Locate and identify every blood parasite.
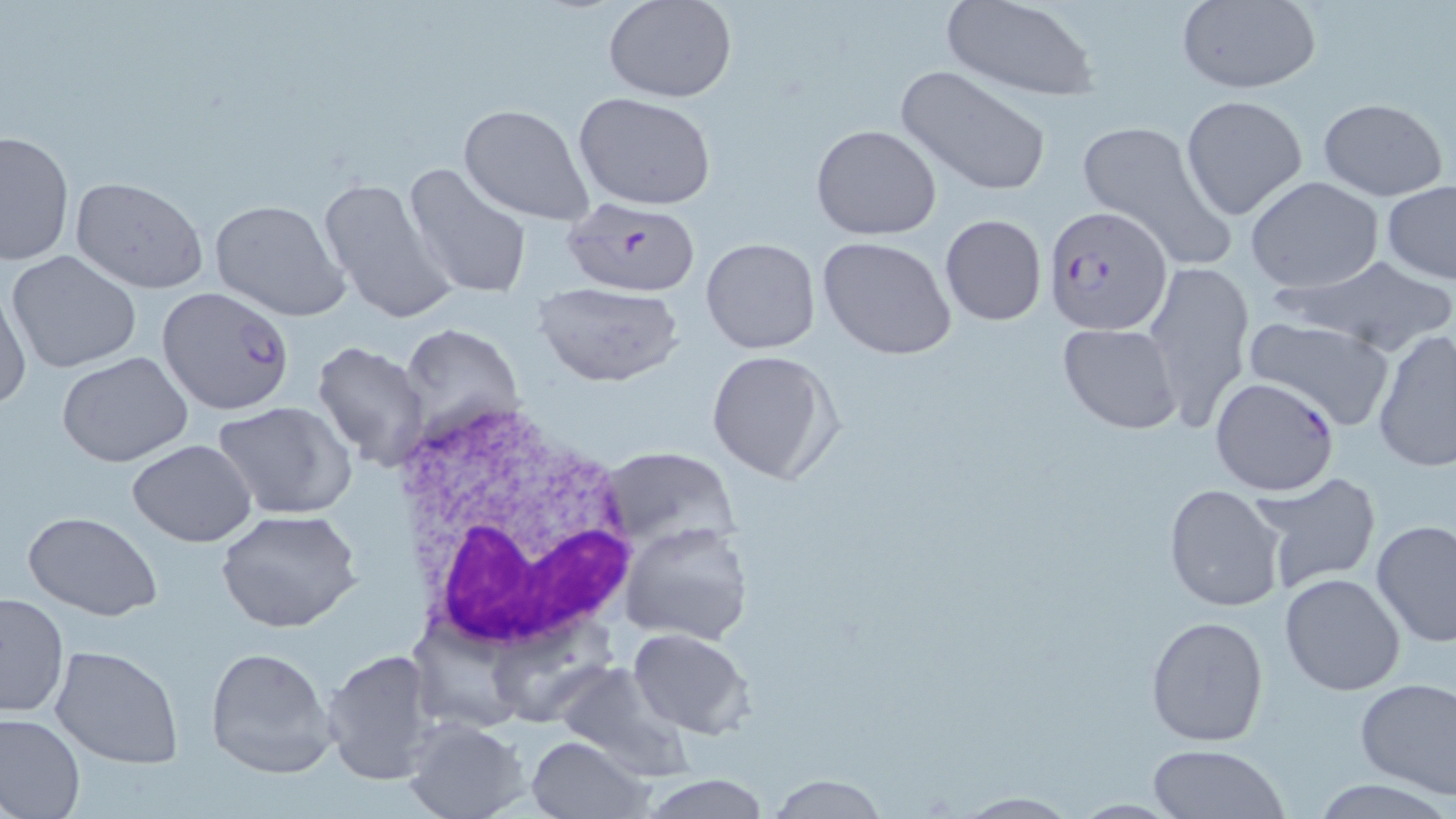

Approximate bounding boxes as named x1/y1/x2/y2 corners in pixels.
Plasmodium falciparum-infected red blood cells (subset): (x1=1045, y1=204, x2=1173, y2=334), (x1=156, y1=286, x2=295, y2=417), (x1=1210, y1=375, x2=1341, y2=497).
No Plasmodium ovale, Plasmodium malariae, Plasmodium vivax, Babesia divergens, or Trypanosoma brucei observed.

Uninfected red blood cell locations (subset): (x1=605, y1=0, x2=736, y2=103), (x1=940, y1=0, x2=1100, y2=102), (x1=1173, y1=1, x2=1322, y2=94), (x1=897, y1=65, x2=1052, y2=198), (x1=573, y1=92, x2=718, y2=209), (x1=1180, y1=94, x2=1308, y2=221), (x1=1317, y1=98, x2=1448, y2=202), (x1=459, y1=103, x2=596, y2=227), (x1=1075, y1=118, x2=1234, y2=269), (x1=811, y1=124, x2=942, y2=240), (x1=0, y1=129, x2=73, y2=267), (x1=400, y1=162, x2=534, y2=301), (x1=317, y1=173, x2=459, y2=324), (x1=69, y1=174, x2=209, y2=294), (x1=1244, y1=176, x2=1386, y2=293), (x1=1382, y1=182, x2=1456, y2=285), (x1=209, y1=199, x2=351, y2=320), (x1=938, y1=213, x2=1048, y2=327), (x1=816, y1=236, x2=957, y2=360), (x1=700, y1=237, x2=820, y2=354), (x1=7, y1=251, x2=143, y2=373), (x1=1289, y1=254, x2=1456, y2=358), (x1=1141, y1=260, x2=1254, y2=429), (x1=530, y1=281, x2=686, y2=388), (x1=0, y1=284, x2=32, y2=410), (x1=1244, y1=315, x2=1397, y2=431), (x1=402, y1=322, x2=524, y2=443), (x1=1057, y1=323, x2=1182, y2=434), (x1=1371, y1=329, x2=1456, y2=473), (x1=313, y1=339, x2=432, y2=474), (x1=705, y1=348, x2=842, y2=486), (x1=57, y1=351, x2=193, y2=467), (x1=214, y1=400, x2=358, y2=520), (x1=127, y1=440, x2=255, y2=548), (x1=599, y1=446, x2=740, y2=549), (x1=1247, y1=472, x2=1381, y2=593), (x1=1163, y1=484, x2=1287, y2=612), (x1=217, y1=509, x2=365, y2=634), (x1=25, y1=512, x2=162, y2=621), (x1=1372, y1=519, x2=1456, y2=647), (x1=618, y1=520, x2=754, y2=645), (x1=1278, y1=572, x2=1407, y2=697), (x1=0, y1=591, x2=68, y2=719), (x1=1146, y1=614, x2=1270, y2=747), (x1=627, y1=628, x2=756, y2=739), (x1=50, y1=643, x2=185, y2=770), (x1=203, y1=645, x2=337, y2=779), (x1=320, y1=646, x2=444, y2=787), (x1=552, y1=663, x2=695, y2=781), (x1=1355, y1=678, x2=1456, y2=799), (x1=0, y1=712, x2=84, y2=819), (x1=400, y1=716, x2=531, y2=819), (x1=525, y1=734, x2=652, y2=819), (x1=1146, y1=744, x2=1289, y2=819), (x1=764, y1=774, x2=889, y2=817), (x1=640, y1=775, x2=774, y2=817), (x1=949, y1=792, x2=1085, y2=817). White blood cell locations: (x1=388, y1=396, x2=645, y2=656). Slide-level diagnosis: Plasmodium falciparum. Thin blood smear. Image is 1456×819 pixels. Single field of view. Light microscopy. May-Grünwald-Giemsa-stained preparation. 1000x magnification.